Report the malaria status of this cell.
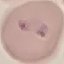
Uninfected.

Summary:
  - Image type: automatically extracted cell patch, resized to 64 × 64 pixels
  - Capture: smartphone camera at the microscope eyepiece
  - Stain: Giemsa
  - Preparation: thin blood film